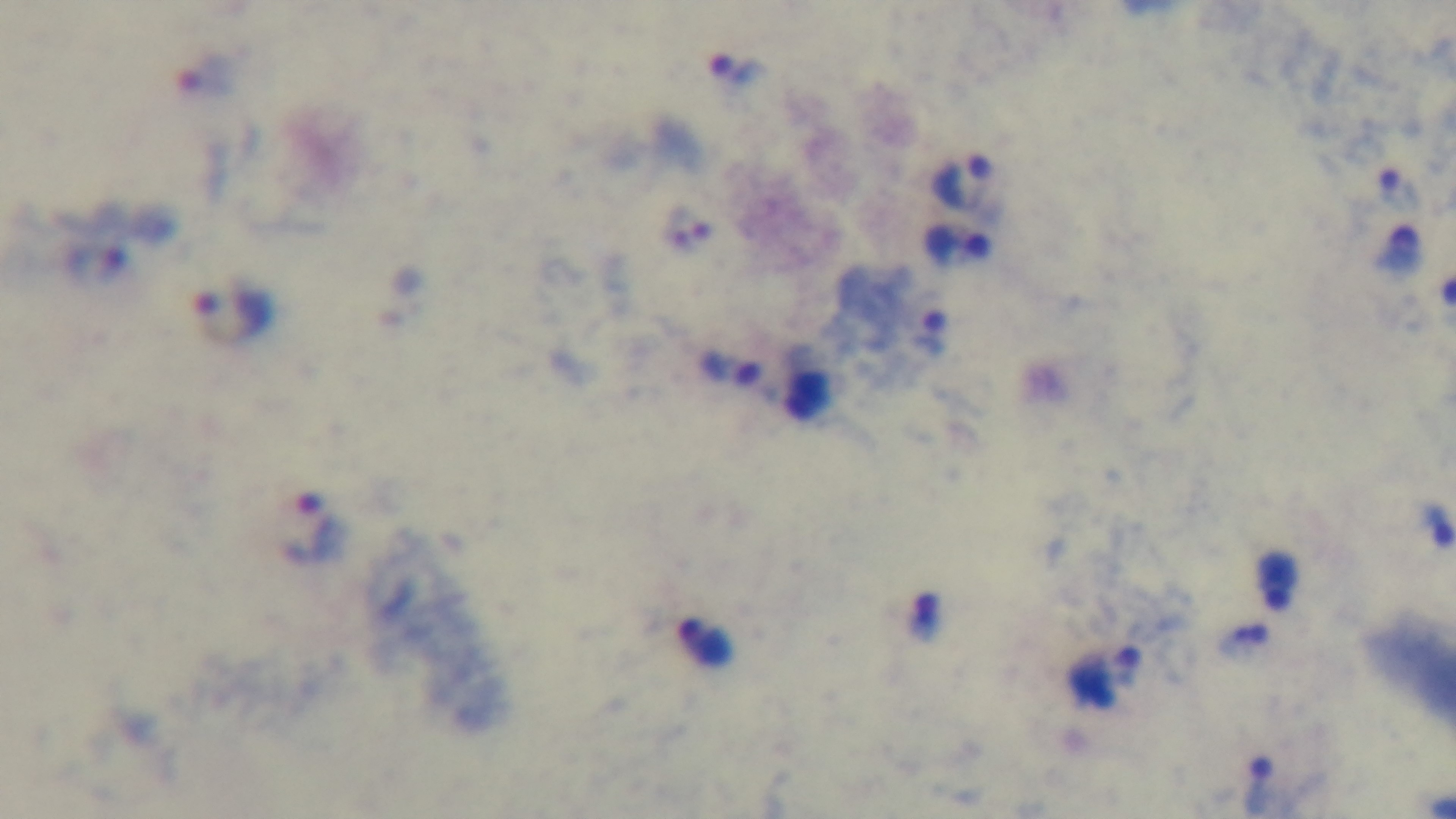 Photomicrograph. Preparation: thick smear. Oil-immersion objective, 100x. Giemsa stain. Mounted 4K digital camera. Malaria status: positive. Single field of view.